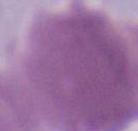

Photomicrograph. A red blood cell is seen. 1000x magnification.